Point out each leukocyte.
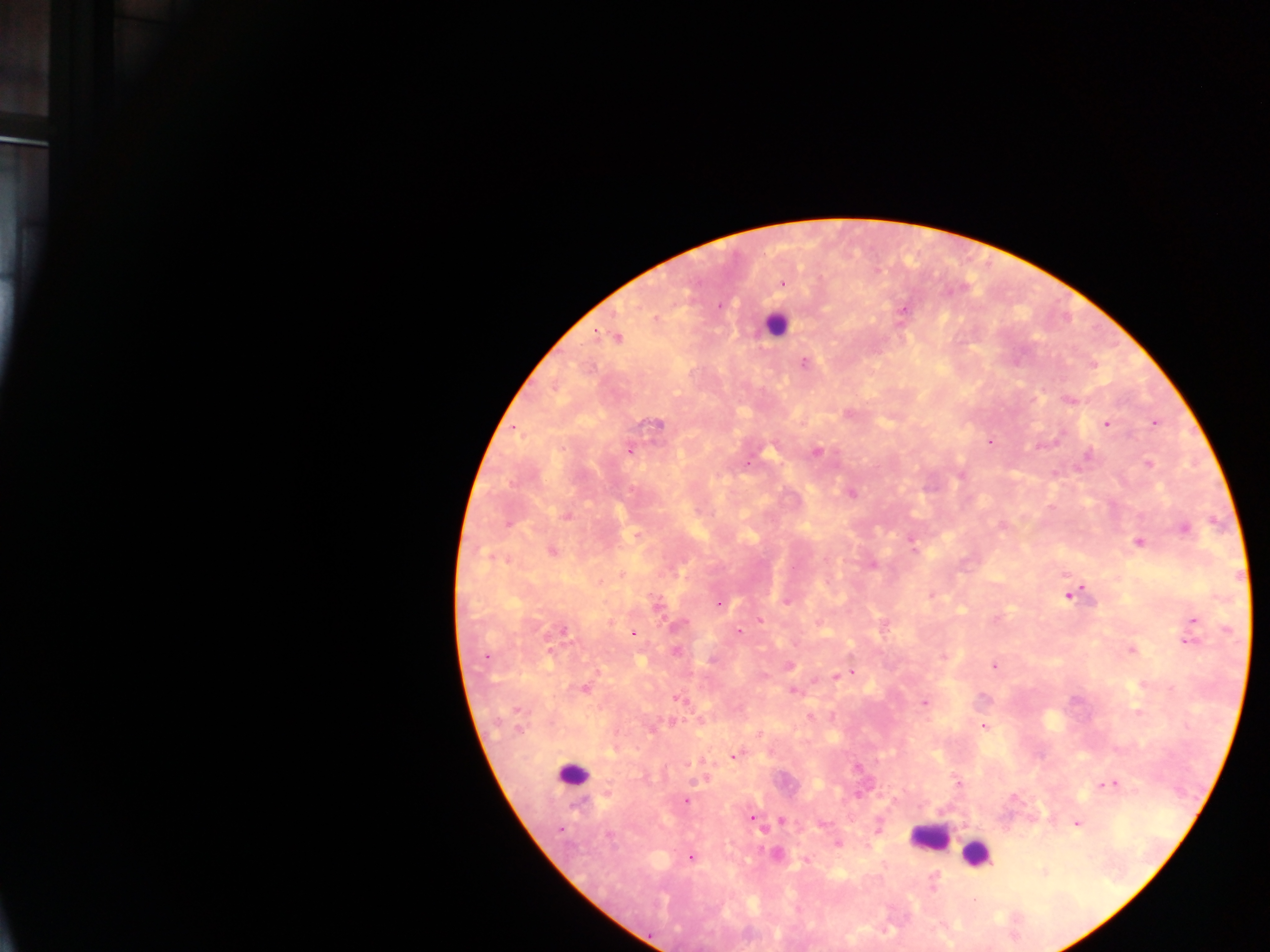

Approximate centers as x y in pixels.
Leukocytes: 774 324; 572 775; 929 837; 977 853.

Malaria parasite locations: 781 283; 718 305; 903 309; 654 318; 616 337; 804 363; 1069 400; 848 413; 1154 422; 1106 423; 656 424; 514 427; 989 441; 630 449; 816 451; 1087 455; 746 464; 1148 464; 960 474; 850 492; 566 515; 508 522; 1001 526; 1184 527; 910 538; 1138 542; 551 550; 914 550; 873 564; 621 574; 1071 593; 787 600; 718 603; 654 604; 759 620; 1192 621; 679 626; 562 631; 738 632; 633 633; 1188 640; 1131 650; 676 651; 485 656; 943 656; 788 664; 994 665; 852 671; 835 675; 584 688; 793 691; 678 697; 924 701; 1137 712; 809 717; 983 726; 758 734; 733 755; 858 768; 703 778; 957 781; 1109 783; 685 801; 752 818; 780 819; 1076 822; 820 824; 836 844; 775 853; 690 856; 805 860; 1043 872; 932 878. Photographed through a microscope with a mobile-phone camera. Image is 1270×952 pixels. Sample from Ghana. Thick blood film. One field of view.